Identify the blood parasite species.
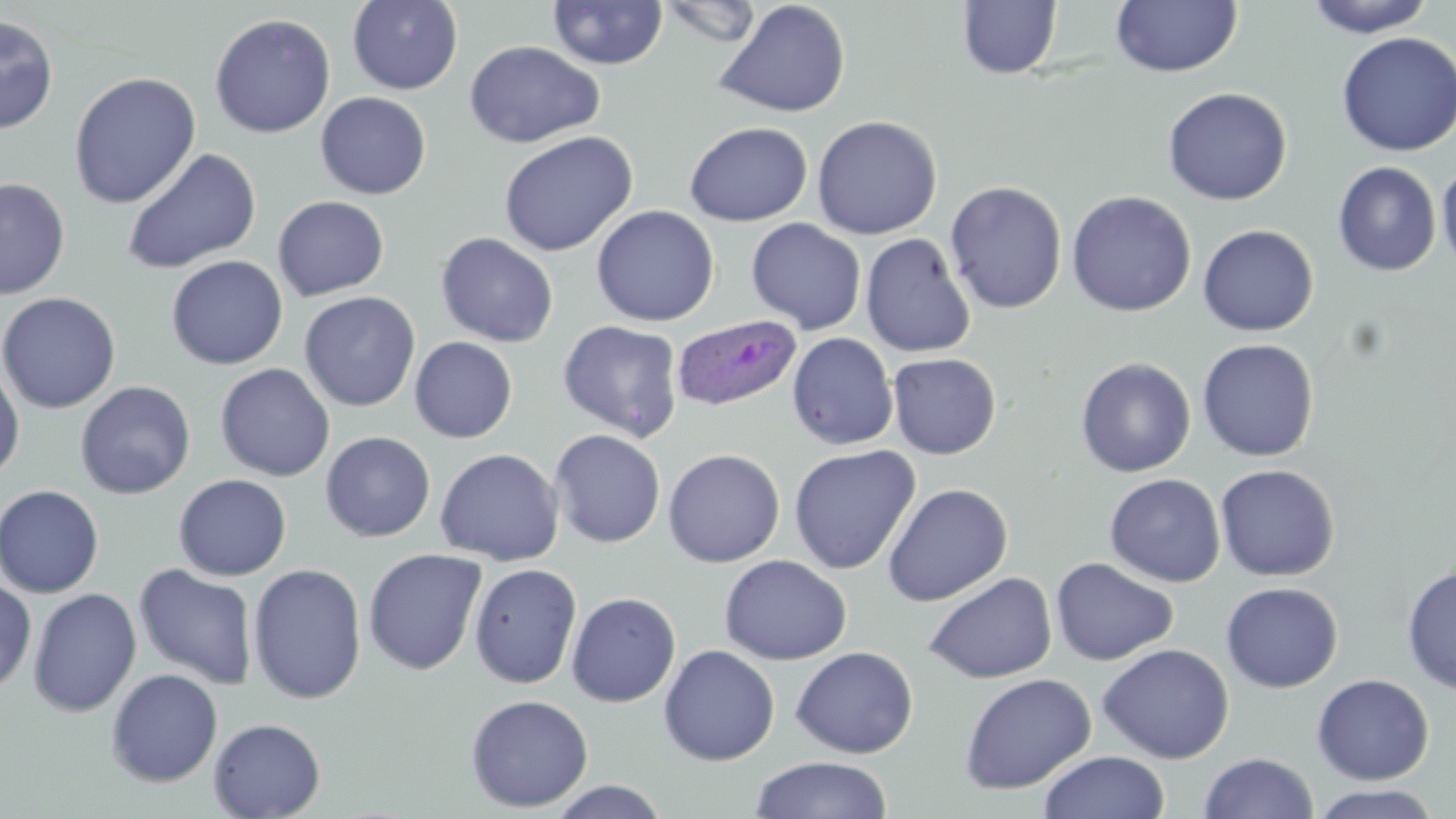

Plasmodium ovale.

Approximate bounding boxes as [x1, y1, x2, y2] in pixels. Uninfected red blood cell locations: [348, 0, 463, 95], [656, 0, 764, 48], [714, 0, 851, 118], [1110, 0, 1242, 78], [1303, 0, 1437, 37], [547, 1, 668, 70], [957, 1, 1062, 79], [0, 13, 58, 135], [210, 13, 336, 139], [1336, 31, 1456, 157], [464, 41, 605, 147], [68, 71, 201, 209], [1162, 87, 1292, 206], [315, 92, 431, 199], [812, 115, 943, 240], [684, 121, 812, 226], [498, 131, 637, 257], [122, 147, 261, 275], [1436, 160, 1456, 272], [1333, 161, 1441, 275], [0, 176, 71, 300], [944, 180, 1067, 315], [1066, 190, 1197, 317], [272, 196, 390, 301], [591, 205, 720, 327], [746, 218, 866, 334], [1197, 224, 1318, 336], [435, 232, 559, 347], [860, 232, 976, 358], [166, 255, 288, 370], [299, 291, 421, 412], [0, 292, 121, 413], [557, 320, 684, 442], [787, 332, 898, 450], [409, 336, 518, 443], [1196, 338, 1320, 462], [887, 352, 1001, 459], [1075, 356, 1196, 477], [0, 359, 25, 484], [214, 363, 336, 482], [75, 381, 195, 499], [549, 428, 666, 548], [320, 431, 435, 542], [789, 444, 920, 575], [435, 448, 564, 566], [663, 448, 785, 567], [1215, 464, 1339, 581], [1105, 473, 1226, 588], [173, 474, 292, 580], [883, 482, 1013, 607], [0, 484, 104, 597], [363, 547, 487, 675], [719, 554, 852, 665], [1050, 557, 1179, 666], [469, 562, 583, 689], [247, 563, 367, 704], [134, 564, 258, 690], [1402, 565, 1456, 694], [924, 572, 1057, 684], [0, 578, 36, 694], [1221, 582, 1344, 693], [28, 588, 141, 717], [566, 592, 681, 707], [1097, 643, 1235, 764], [659, 644, 780, 765], [791, 645, 919, 758], [106, 668, 223, 788], [959, 673, 1096, 795], [1311, 673, 1434, 784], [465, 694, 594, 812], [208, 717, 326, 818], [1039, 751, 1170, 819], [1199, 752, 1320, 818], [750, 755, 894, 818], [546, 780, 672, 818], [1307, 784, 1444, 819]. Plasmodium ovale-infected red blood cell locations: [671, 314, 803, 412]. Thin blood smear. Light microscopy. May-Grünwald-Giemsa-stained preparation. 1000x magnification. Image is 1456×819 pixels. One field of a larger specimen.